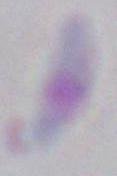

modality: micrograph
identification: Toxoplasma gondii
magnification: 1000x